Classify this cell by malaria status.
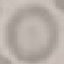
Uninfected.

Summary:
  - Preparation: thin smear
  - Capture: smartphone through the microscope eyepiece
  - Image type: cell patch, automatically extracted from a larger field of view and resized to 64 × 64 pixels
  - Stain: Giemsa